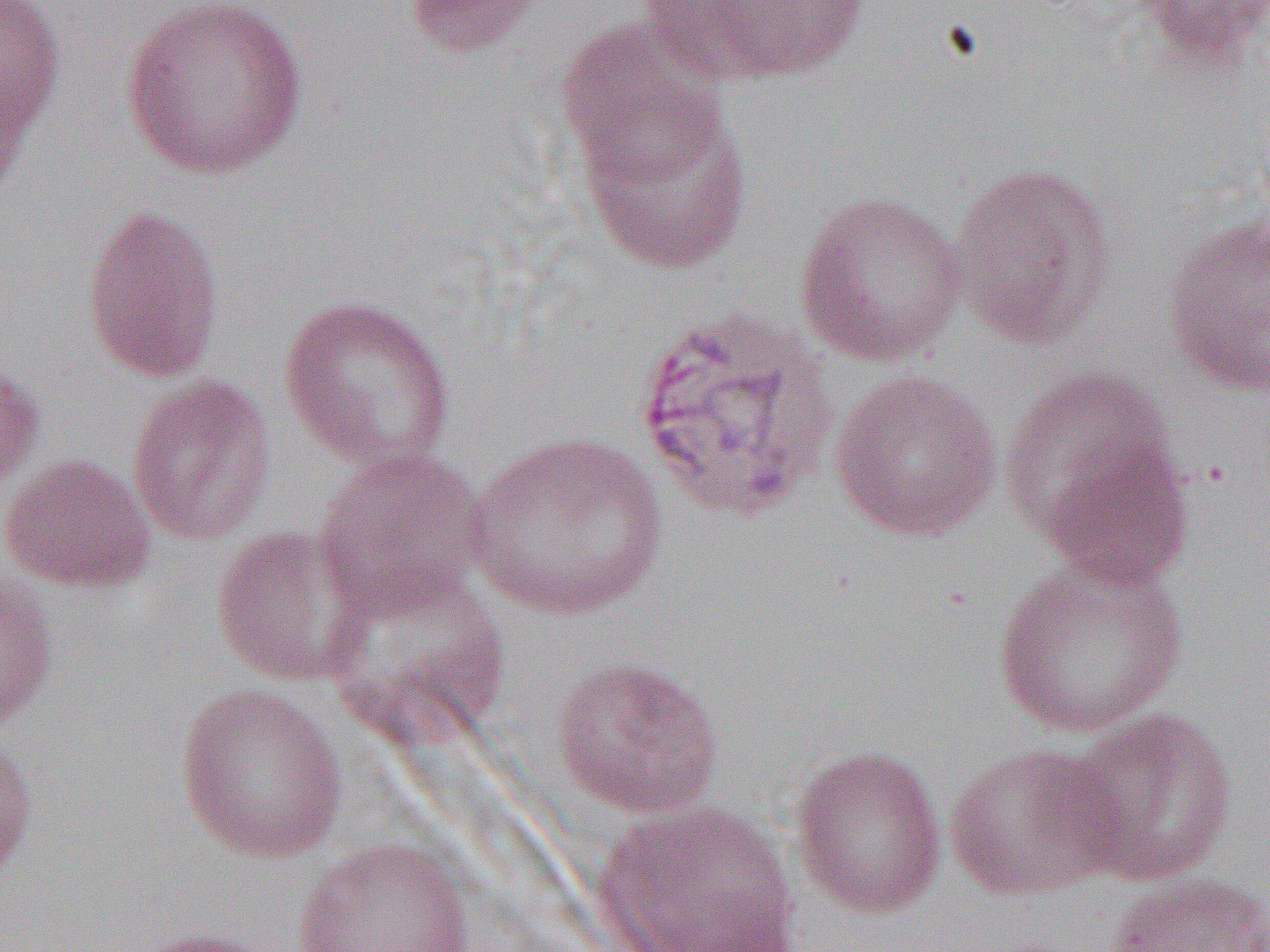
Summary:
  - Coordinate format: approximate bounding boxes as (x1, y1, x2, y2) in pixels
  - Uninfected red blood cell locations: (0, 0, 66, 156), (119, 0, 308, 180), (402, 0, 546, 58), (656, 0, 870, 83), (1130, 1, 1270, 69), (554, 19, 727, 184), (0, 64, 30, 205), (577, 92, 754, 275), (947, 161, 1117, 349), (793, 188, 968, 367), (81, 204, 225, 384), (1164, 214, 1270, 398), (278, 293, 457, 474), (0, 359, 45, 497), (1000, 362, 1180, 537), (827, 369, 1003, 543), (125, 373, 277, 546), (465, 431, 669, 622), (1039, 439, 1194, 592), (313, 446, 496, 620), (0, 453, 156, 594), (208, 524, 371, 686), (993, 553, 1188, 739), (319, 563, 510, 745), (0, 565, 60, 732), (550, 654, 725, 820), (174, 683, 347, 863), (1063, 707, 1239, 887), (0, 731, 39, 885), (942, 742, 1125, 900), (788, 743, 948, 920), (590, 800, 802, 952), (292, 836, 474, 952), (1103, 872, 1270, 952), (120, 926, 280, 952)
  - Slide-level diagnosis: Plasmodium vivax
  - Modality: optical microscopy
  - Field of view: one of a larger specimen
  - Magnification: 1000x
  - Image size: 1270×952 pixels
  - Preparation: thin blood film